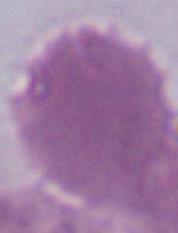

Summary:
  - Modality: micrograph
  - Identification: red blood cell
  - Magnification: 1000x